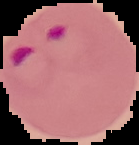

Malaria status: parasitized. Image is 139×145 pixels. From a thin blood smear. Segmented cell region on a black background.